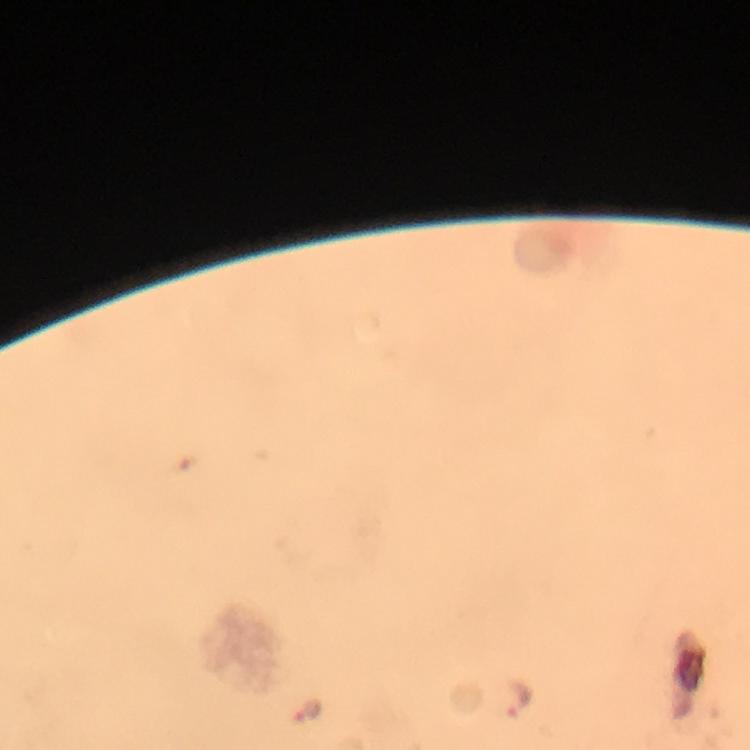 Approximate object centers, in pixels from the top-left corner. Plasmodium parasite locations: (x=516, y=699), (x=306, y=709). From a malaria diagnostic workup. Giemsa-stained preparation. Immersion oil applied. At 100x magnification. Thick blood smear. Image is 750×750 pixels. A crop from one field of view. Smartphone photograph taken through a microscope.